Outline each Plasmodium falciparum-infected red blood cell.
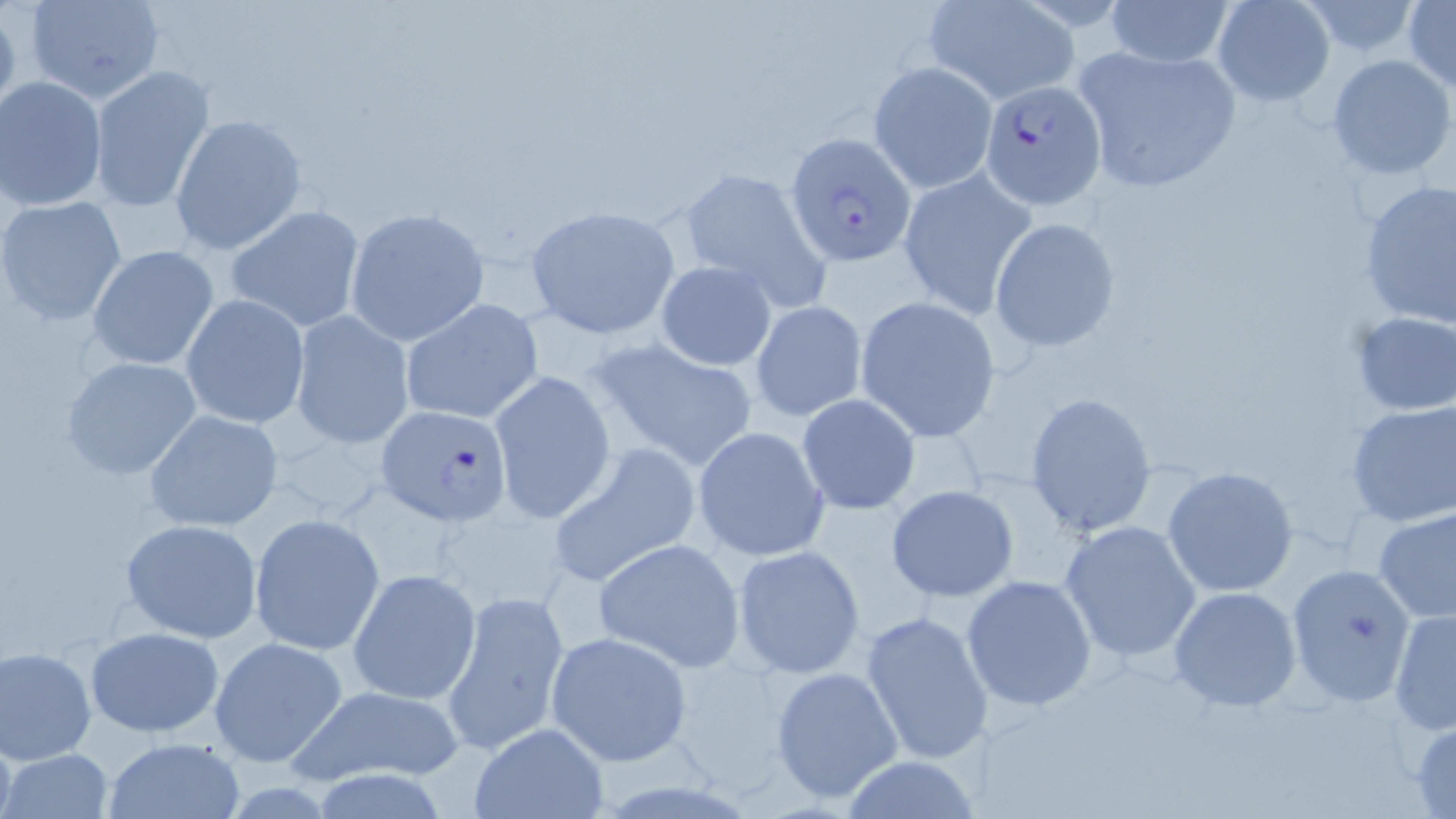
Approximate bounding boxes as (x1,y1)-(x2,y2) corner pairs in pixels.
Plasmodium falciparum-infected red blood cells: (979,79)-(1105,209), (788,133)-(916,264), (376,404)-(513,525).

Summary:
  - Uninfected red blood cell locations: (24,0)-(167,105), (1105,0)-(1235,70), (1211,0)-(1336,107), (1403,0)-(1456,92), (924,1)-(1078,103), (1296,1)-(1427,58), (1068,43)-(1246,195), (1326,54)-(1454,180), (867,61)-(997,193), (87,63)-(216,213), (1,77)-(111,214), (170,113)-(308,255), (677,165)-(830,308), (899,166)-(1036,318), (1359,179)-(1455,333), (1,199)-(128,326), (226,203)-(366,333), (526,205)-(681,339), (347,207)-(487,348), (988,217)-(1119,353), (87,244)-(219,371), (655,260)-(778,371), (181,293)-(308,429), (855,297)-(999,439), (400,298)-(544,427), (749,300)-(869,423), (289,310)-(415,451), (1347,310)-(1456,419), (589,338)-(762,471), (60,355)-(203,481), (487,370)-(615,523), (1023,390)-(1158,539), (796,394)-(921,516), (1345,401)-(1455,528), (142,409)-(284,533), (692,425)-(829,563), (549,444)-(702,586), (1162,465)-(1297,597), (884,484)-(1020,603), (1374,506)-(1456,625), (249,512)-(386,655), (119,518)-(265,642), (1056,521)-(1202,664), (594,538)-(745,672), (732,545)-(866,679), (1285,561)-(1418,707), (349,568)-(481,704), (961,575)-(1098,710), (1169,586)-(1302,712), (441,589)-(570,755), (1389,607)-(1455,735), (861,611)-(994,767), (82,627)-(227,735), (545,633)-(692,765), (209,635)-(349,768), (0,645)-(97,764), (768,666)-(905,805), (284,683)-(470,787), (1409,718)-(1456,819), (465,722)-(610,818), (102,737)-(245,819), (4,748)-(110,817), (838,755)-(981,819)
  - Slide-level diagnosis: Plasmodium falciparum
  - Image size: 1456×819 pixels
  - Magnification: 1000x
  - Stain: May-Grünwald-Giemsa
  - Field of view: single
  - Preparation: thin blood film
  - Modality: light microscopy